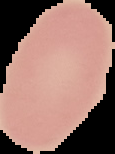 Result: negative for Plasmodium parasites. Image is 115×154 pixels. From a thin blood film. Cell region segmented out of the field of view; the surrounding area is masked to black.